Comment on the morphology of the red blood cells.
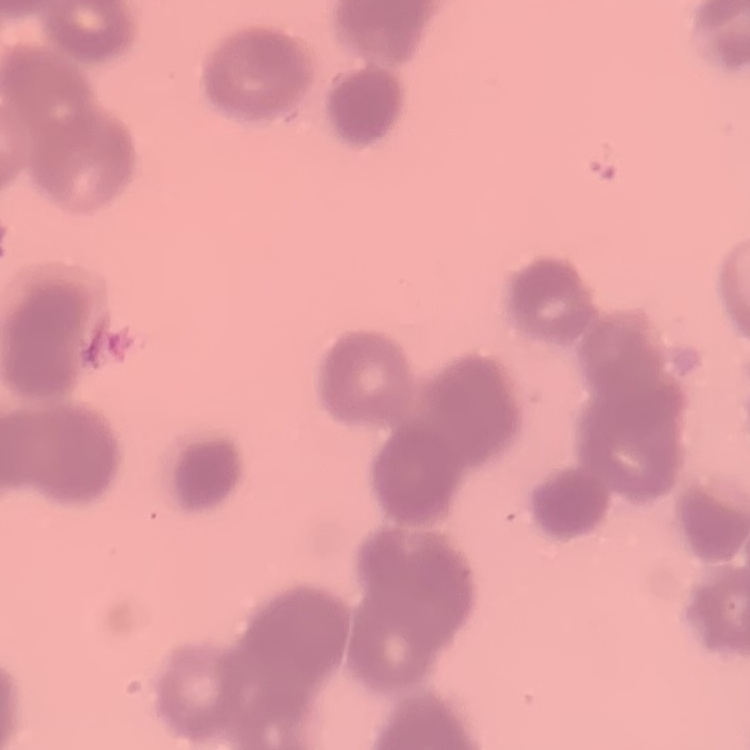

They show rouleaux formation.

Field's or Giemsa stain. Square crop of a larger photomicrograph. Thin blood film.